Describe the morphology of the erythrocytes.
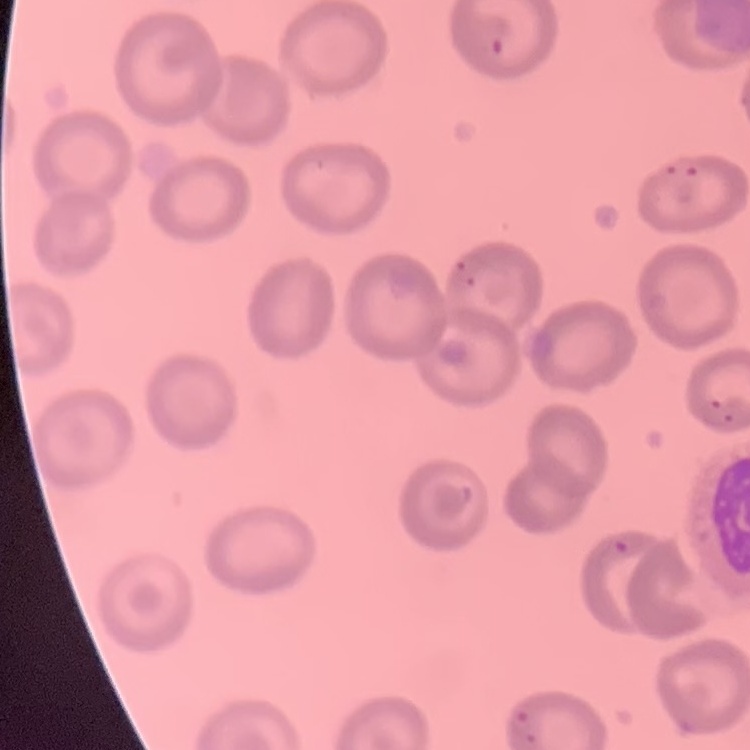
No rouleaux formation.

preparation = thin peripheral smear
stain = Field's or Giemsa
image type = one tile cut from a larger photomicrograph